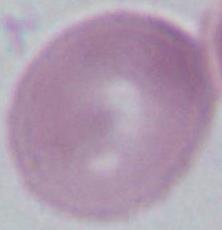
magnification = 400x or 1000x
modality = micrograph
identification = Plasmodium